Describe the morphology of the red blood cells.
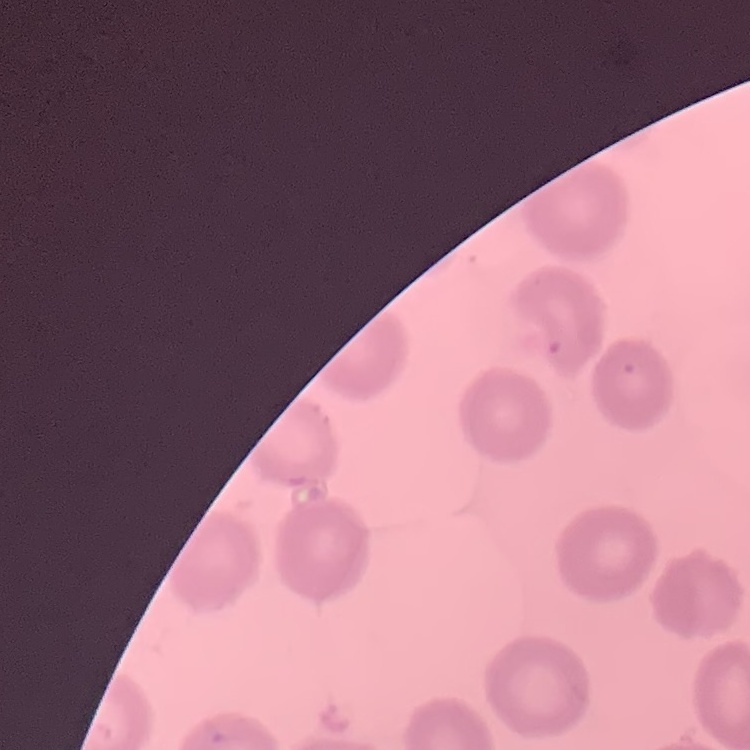
They show no rouleaux formation.

Summary:
  - Stain: Field's or Giemsa
  - Preparation: thin peripheral smear
  - Image type: one tile cut from a larger photomicrograph